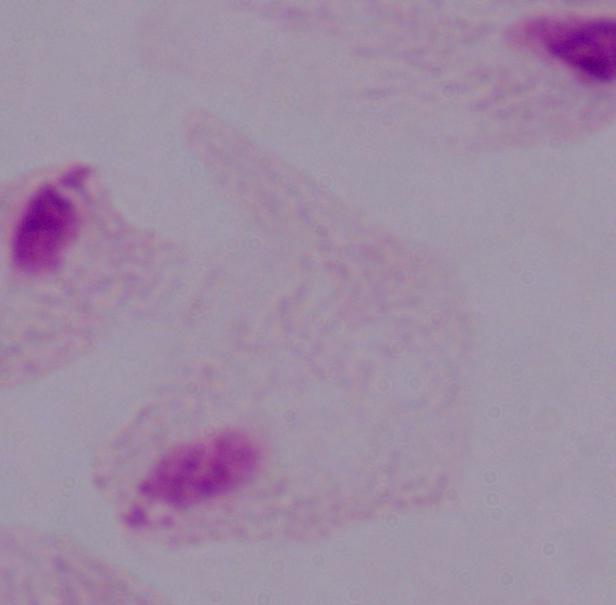

magnification: 1000x
identification: trichomonad
modality: micrograph